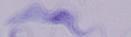

{
  "modality": "micrograph",
  "identification": "trypanosome",
  "magnification": "1000x"
}